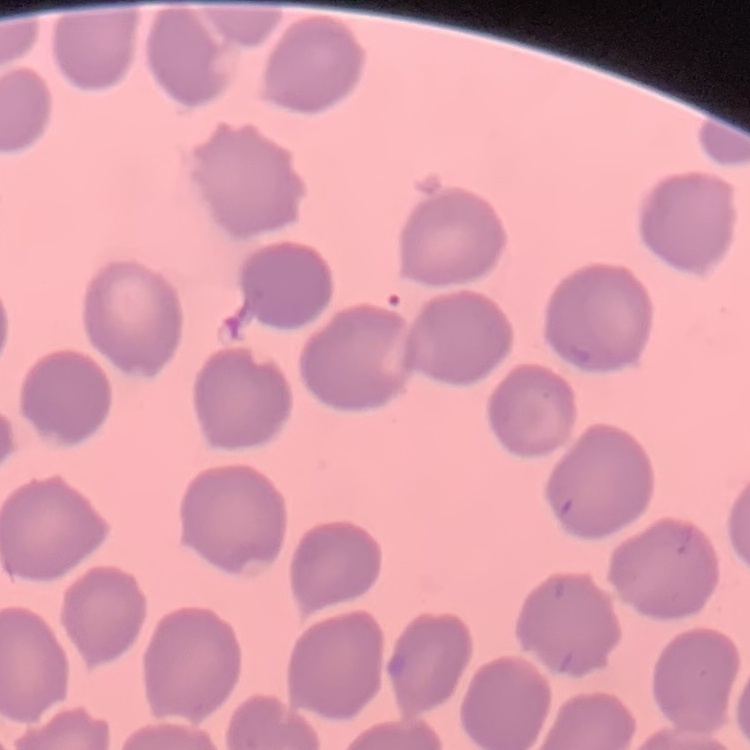
Summary:
  - Red blood cell morphology: no rouleaux formation
  - Preparation: thin blood smear
  - Image type: one tile cut from a larger photomicrograph
  - Stain: Field's or Giemsa